Assess for Plasmodium parasites.
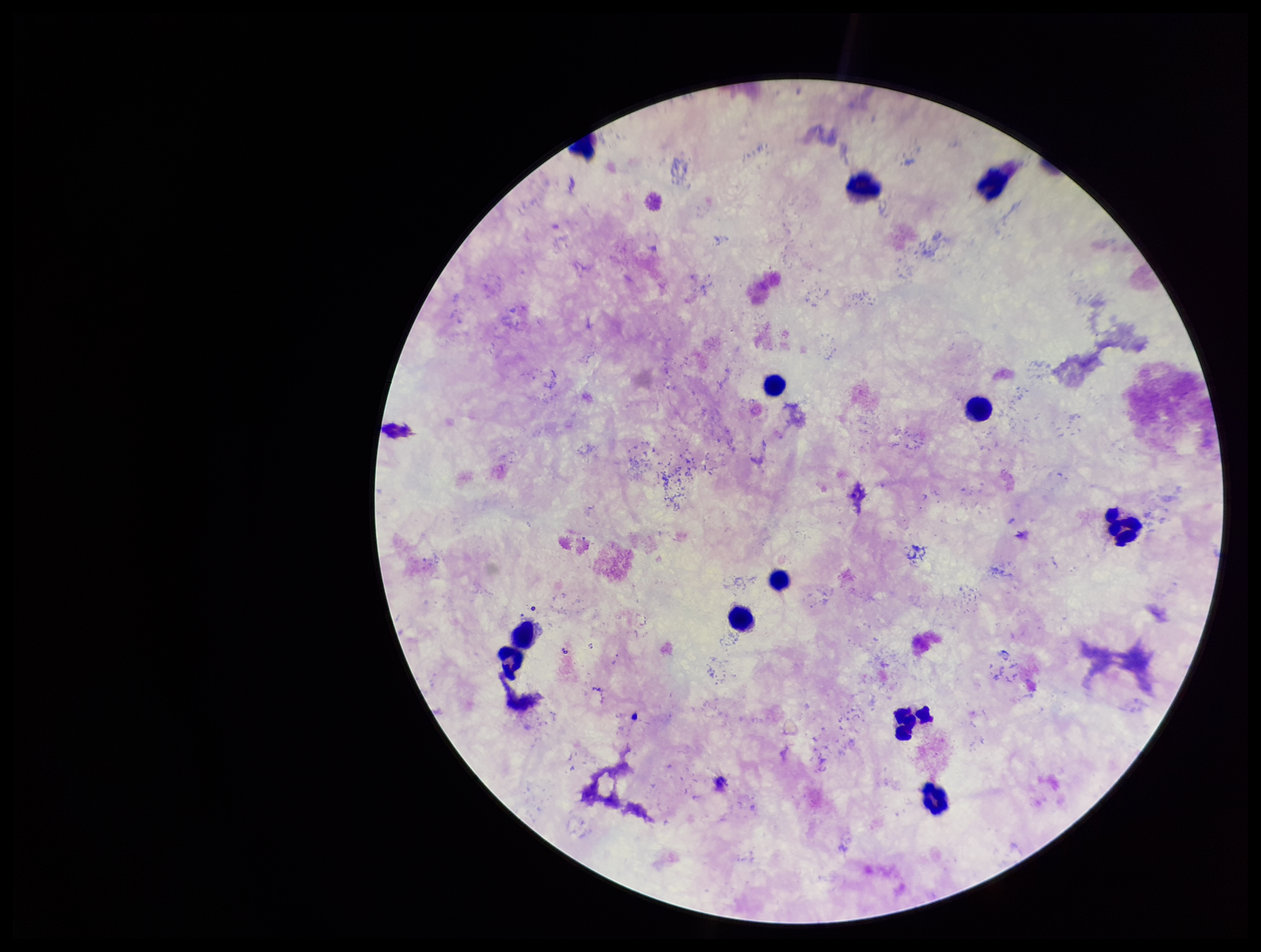
None identified.

Summary:
  - Stain: Giemsa
  - Capture: smartphone photograph through the microscope eyepiece
  - Preparation: thick blood smear
  - Field of view: one from this slide
  - Patient malaria status: negative
  - Leukocyte count: 10
  - Image size: 1261×952 pixels
  - Parasite count: 0